Name the parasite shown.
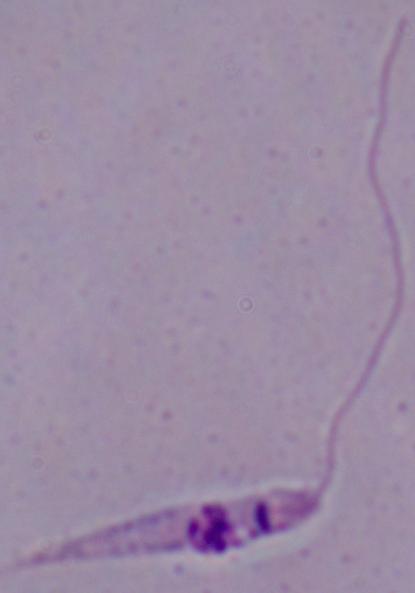

Leishmania.

Summary:
  - Modality: photomicrograph
  - Magnification: 1000x